Assess this cell for malaria.
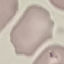
Uninfected.

Giemsa-stained preparation. Acquired by smartphone through the microscope eyepiece. Thin smear of blood. Automatically extracted cell patch, resized to 64 × 64 pixels.